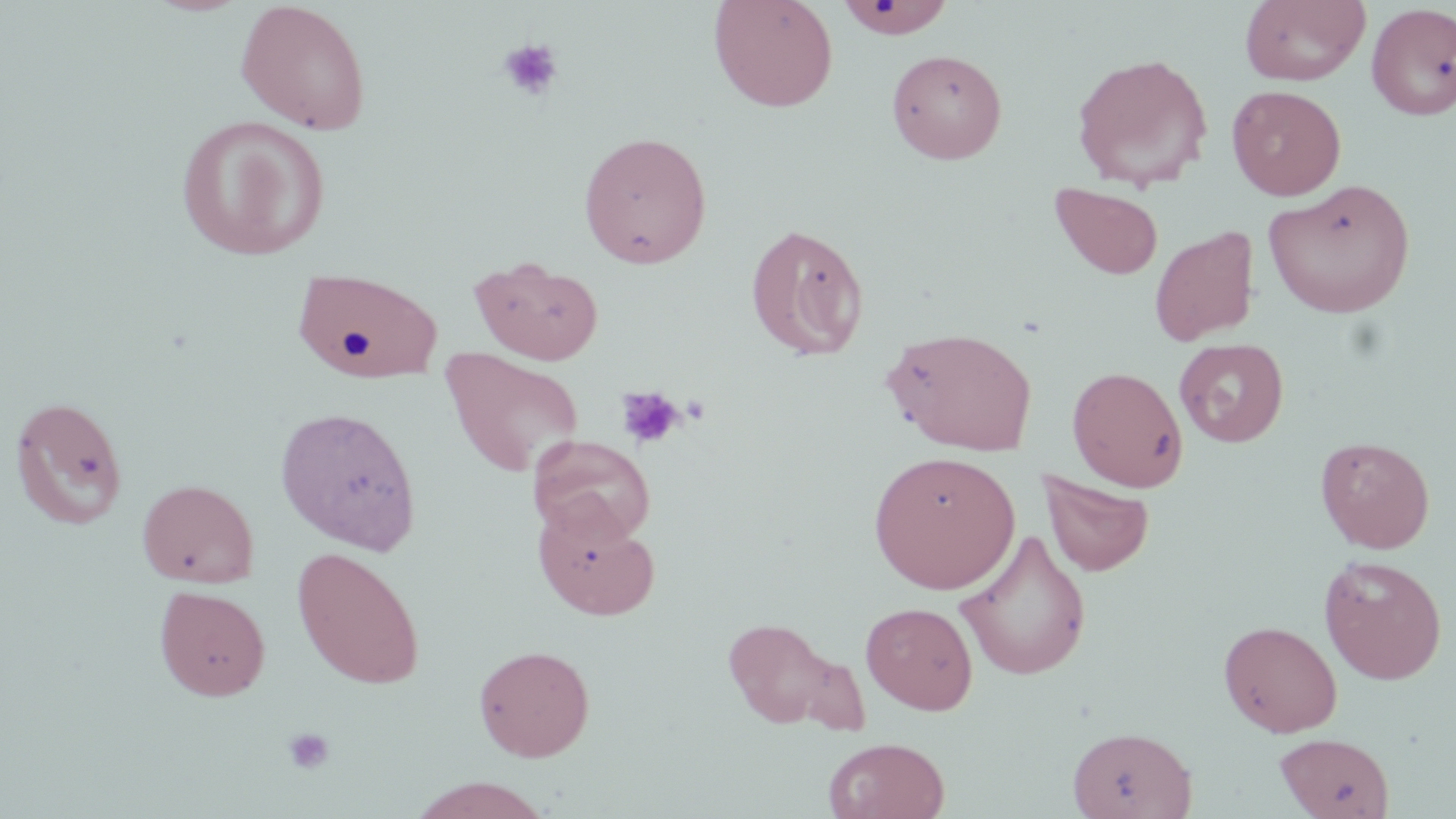 Approximate bounding boxes as [x1, y1, x2, y2] in pixels. Uninfected red blood cell locations: [235, 0, 372, 135], [708, 0, 839, 113], [1240, 0, 1371, 86], [835, 1, 955, 39], [1366, 3, 1456, 121], [887, 48, 1007, 164], [1071, 52, 1213, 190], [1226, 85, 1346, 200], [176, 114, 330, 261], [578, 130, 713, 268], [1263, 178, 1417, 319], [1050, 183, 1164, 281], [745, 222, 869, 362], [1150, 225, 1259, 346], [470, 255, 604, 365], [294, 267, 444, 380], [882, 325, 1038, 456], [1174, 337, 1290, 447], [439, 349, 585, 478], [1067, 366, 1188, 491], [9, 395, 129, 530], [275, 405, 422, 554], [529, 435, 656, 545], [1316, 436, 1435, 553], [869, 450, 1020, 594], [1040, 470, 1155, 578], [137, 478, 259, 588], [533, 501, 660, 621], [957, 527, 1092, 682], [292, 546, 426, 690], [1319, 554, 1447, 684], [154, 585, 271, 702], [861, 601, 978, 714], [721, 616, 844, 730], [1218, 619, 1342, 737], [473, 644, 595, 762], [1068, 725, 1196, 819], [1274, 732, 1395, 819], [823, 736, 949, 819], [408, 776, 555, 819]. Platelet locations: [497, 39, 564, 102], [615, 386, 686, 450], [283, 727, 336, 775]. Slide-level diagnosis: negative for blood parasites. Captured at 1000x magnification. Single field of view. Light microscopy. Thin blood film. May-Grünwald-Giemsa-stained preparation. Image is 1456×819 pixels.